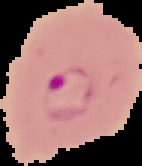

The area outside the segmented cell region is set to black. Image is 142×166 pixels. From a thin blood smear. Result: Plasmodium parasites identified.